Report the malaria status of this cell.
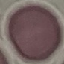

Uninfected.

Summary:
  - Stain: Giemsa
  - Image type: cell patch, automatically extracted from a larger field of view and resized to 64 × 64 pixels
  - Capture: smartphone camera at the microscope eyepiece
  - Preparation: thin blood film